Give the preparation type.
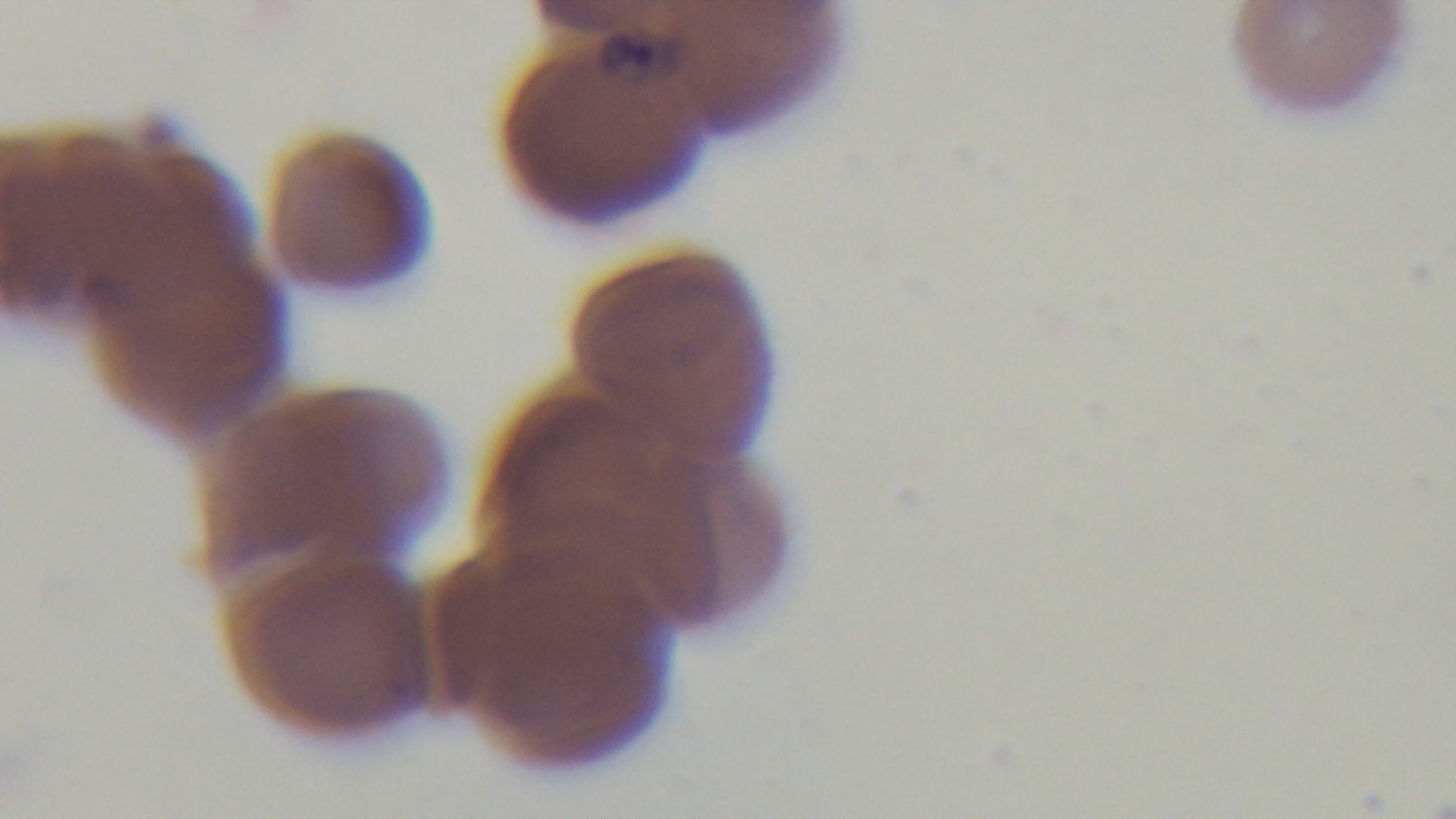

It is a thin blood film.

Single field of view. Malaria status: infected. Photomicrograph. Giemsa stain. Captured with a mounted 4K digital camera. 100x oil-immersion objective.